Report the malaria status of this cell.
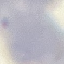
Uninfected.

Automatically extracted cell patch, resized to 64 × 64 pixels. Acquired by smartphone through the microscope eyepiece. Thin blood smear. Giemsa-stained preparation.